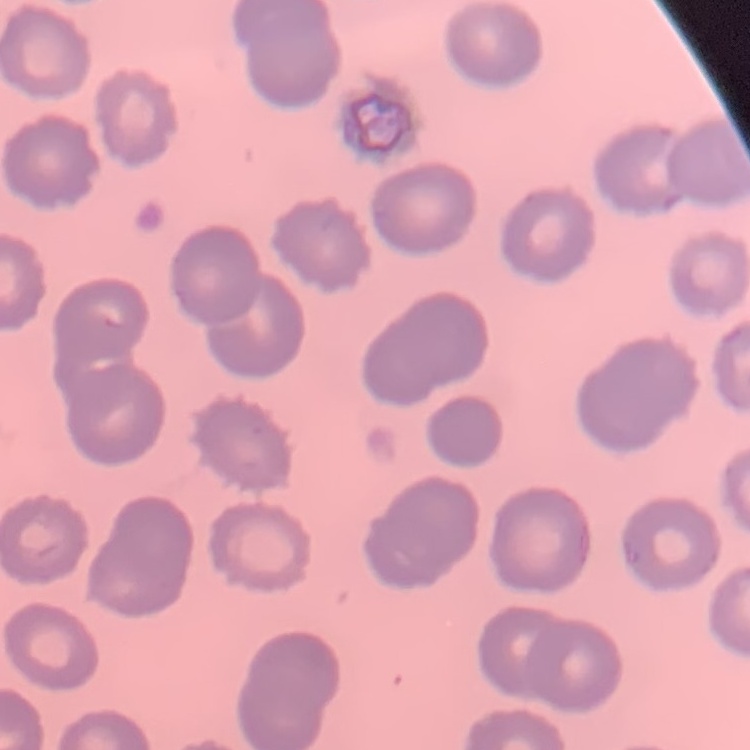

erythrocyte_morphology: no rouleaux formation
image_type: square crop of a larger photomicrograph
stain: Field's or Giemsa
preparation: thin blood film